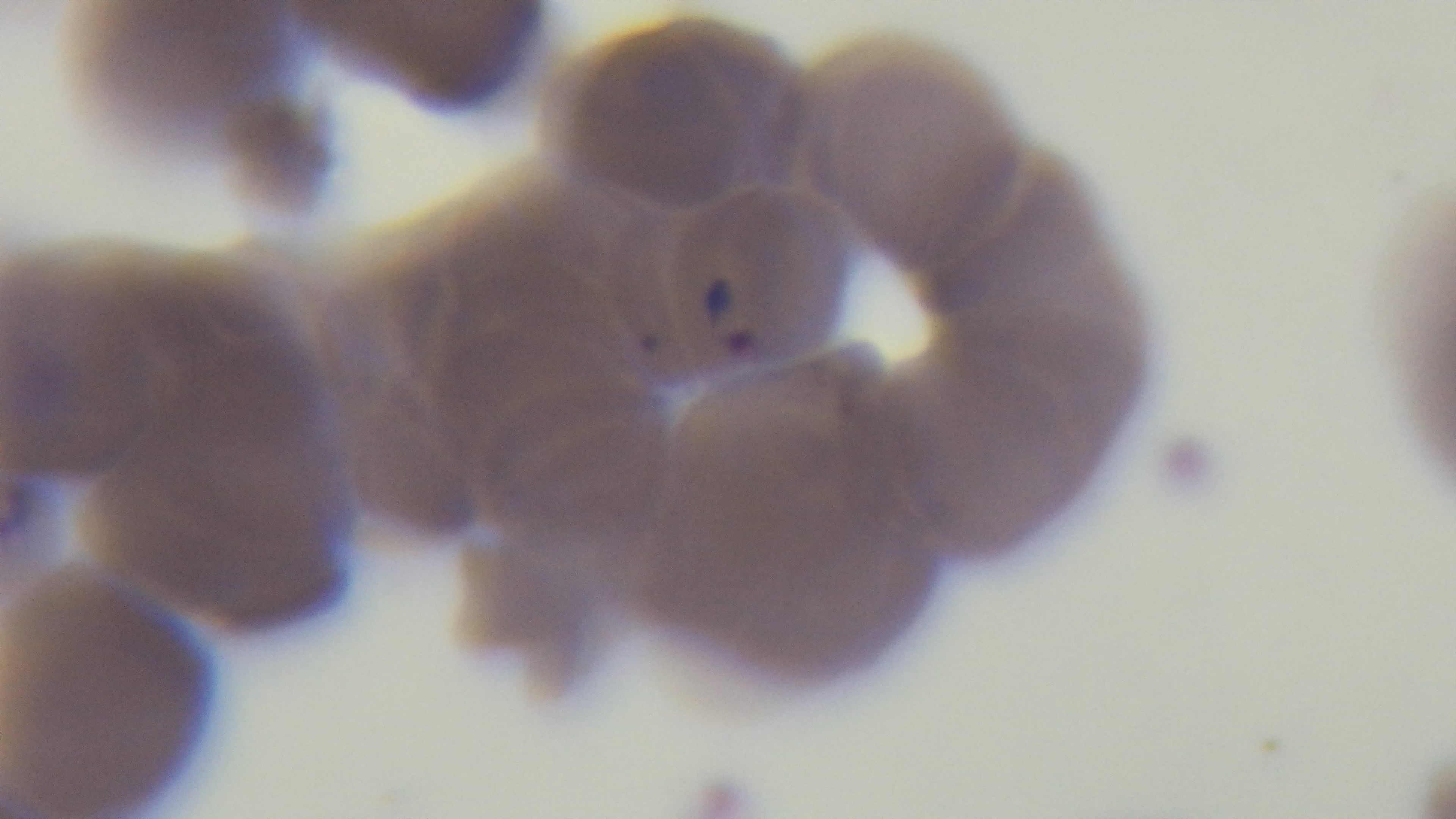 Oil-immersion objective, 100x. Preparation: thin. Photomicrograph. One field from the slide. Giemsa stain. Captured with a mounted 4K digital camera. Malaria status: positive.